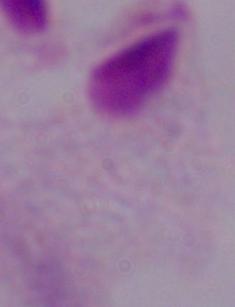 Micrograph. 1000x magnification. A trichomonad is shown.